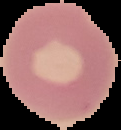

malaria_status: uninfected
image_type: segmented cell region on a black background
image_size: 121×130 pixels
preparation: thin blood film